Assess the morphology of the erythrocytes.
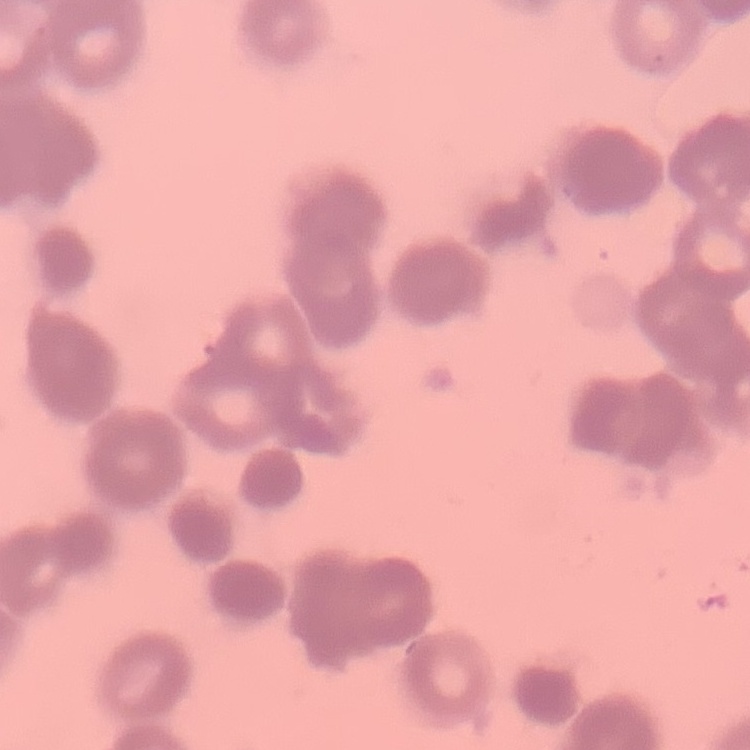

Rouleaux formation.

Thin blood film. Stained with either Field's or Giemsa. Square crop of a larger photomicrograph.